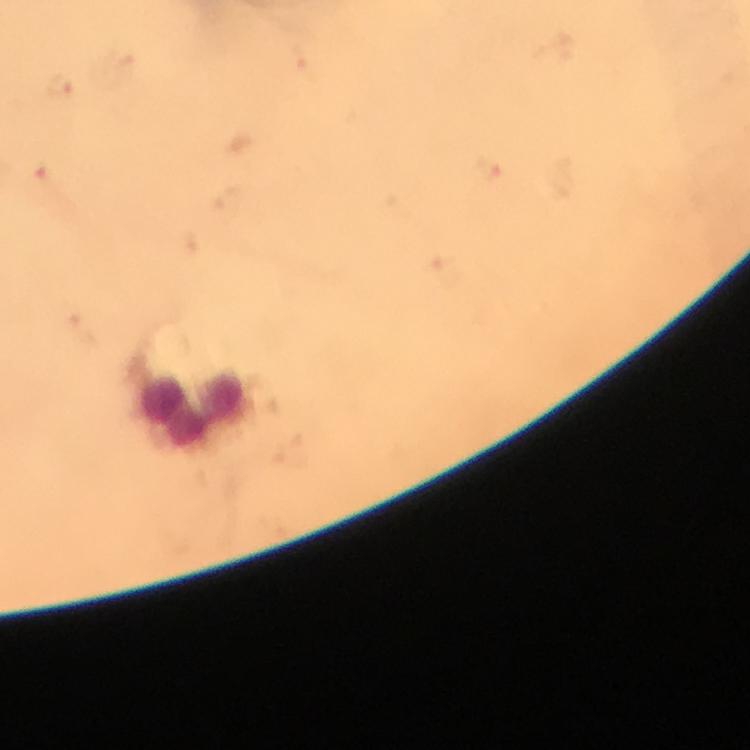

{
  "immersion_oil": "used",
  "image_size": "750×750 pixels",
  "preparation": "thick smear",
  "context": "from a malaria diagnostic workup",
  "stain": "Giemsa",
  "magnification": "100x",
  "plasmodium_parasite_locations": "approximate object centers, in pixels from the top-left corner: (x=59, y=85), (x=489, y=171), (x=41, y=177)",
  "cropped_from": "one field of view",
  "leukocyte_locations": "approximate object centers, in pixels from the top-left corner: (x=192, y=404)",
  "capture": "smartphone camera through the microscope"
}